Classify this cell by malaria status.
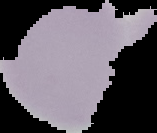
Uninfected.

Cell region segmented out of the field of view; the surrounding area is masked to black. Image is 157×133 pixels. From a thin blood film.